Assess this cell for malaria.
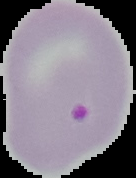
Parasitized.

From a thin blood smear. Image is 136×178 pixels. The area outside the segmented cell region is set to black.